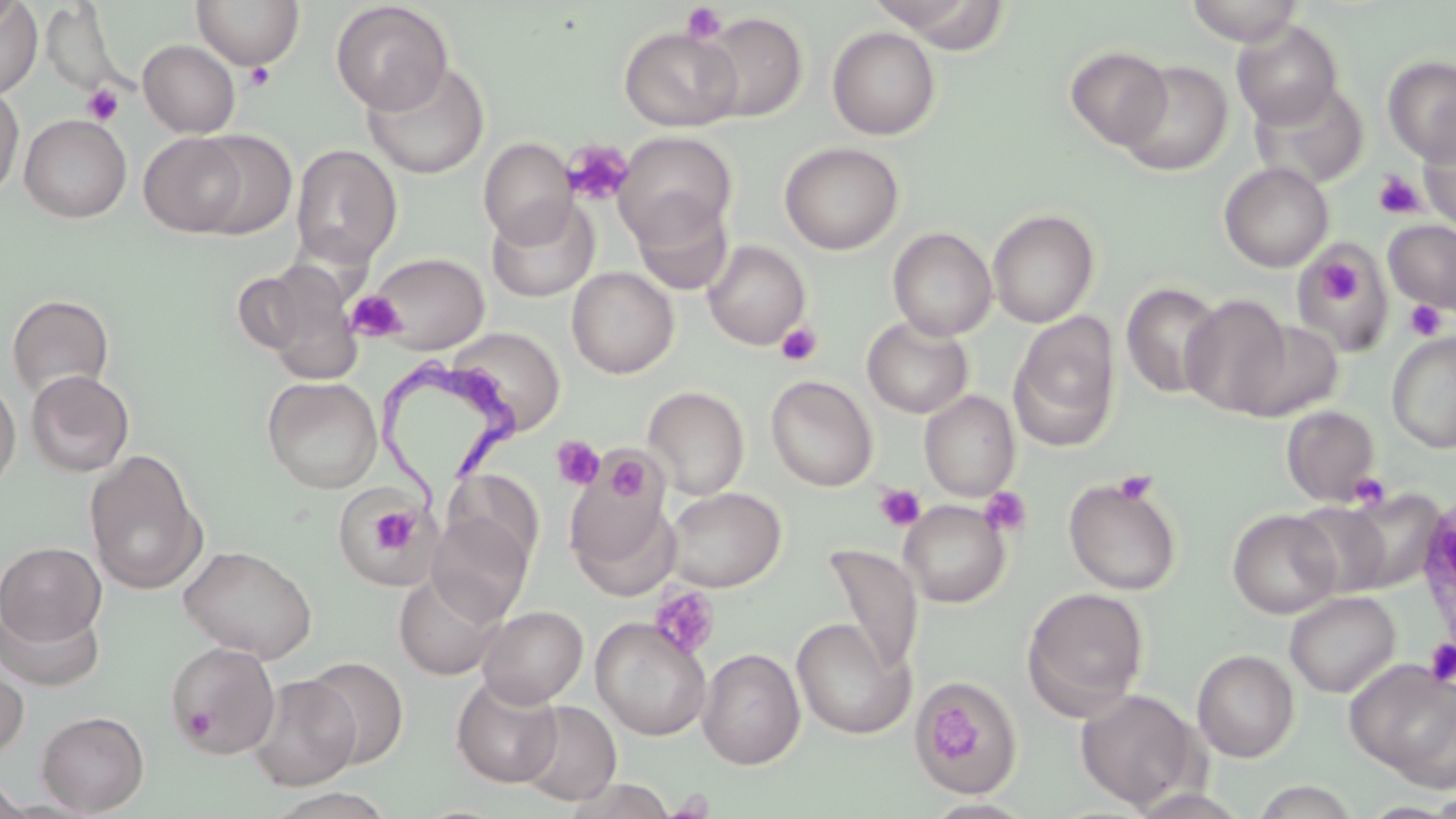 Approximate bounding boxes as named x1/y1/x2/y2 corners in pixels. Uninfected red blood cell locations: (x1=191, y1=0, x2=305, y2=70), (x1=867, y1=0, x2=1011, y2=50), (x1=0, y1=1, x2=42, y2=99), (x1=0, y1=1, x2=24, y2=31), (x1=331, y1=1, x2=453, y2=115), (x1=1183, y1=1, x2=1306, y2=46), (x1=43, y1=6, x2=122, y2=95), (x1=697, y1=11, x2=807, y2=123), (x1=1230, y1=19, x2=1344, y2=128), (x1=618, y1=26, x2=743, y2=131), (x1=827, y1=26, x2=941, y2=140), (x1=138, y1=40, x2=241, y2=138), (x1=1065, y1=45, x2=1173, y2=151), (x1=1383, y1=55, x2=1456, y2=165), (x1=361, y1=60, x2=490, y2=179), (x1=1118, y1=60, x2=1233, y2=176), (x1=1249, y1=80, x2=1368, y2=188), (x1=0, y1=84, x2=25, y2=202), (x1=19, y1=114, x2=132, y2=223), (x1=1418, y1=123, x2=1456, y2=233), (x1=190, y1=130, x2=297, y2=239), (x1=139, y1=132, x2=249, y2=237), (x1=613, y1=132, x2=737, y2=245), (x1=478, y1=138, x2=577, y2=245), (x1=779, y1=142, x2=904, y2=255), (x1=290, y1=144, x2=402, y2=268), (x1=1219, y1=162, x2=1333, y2=272), (x1=630, y1=193, x2=734, y2=296), (x1=485, y1=197, x2=599, y2=303), (x1=987, y1=208, x2=1099, y2=328), (x1=1383, y1=219, x2=1456, y2=314), (x1=888, y1=227, x2=997, y2=341), (x1=703, y1=240, x2=811, y2=350), (x1=1293, y1=248, x2=1393, y2=354), (x1=369, y1=252, x2=490, y2=353), (x1=242, y1=260, x2=363, y2=379), (x1=566, y1=267, x2=679, y2=379), (x1=1121, y1=281, x2=1225, y2=400), (x1=7, y1=292, x2=115, y2=399), (x1=1180, y1=294, x2=1292, y2=417), (x1=1008, y1=311, x2=1121, y2=452), (x1=862, y1=317, x2=973, y2=418), (x1=1231, y1=319, x2=1343, y2=422), (x1=448, y1=326, x2=566, y2=435), (x1=1387, y1=332, x2=1456, y2=453), (x1=25, y1=369, x2=135, y2=477), (x1=766, y1=375, x2=877, y2=492), (x1=263, y1=376, x2=383, y2=493), (x1=0, y1=377, x2=21, y2=496), (x1=641, y1=384, x2=874, y2=495), (x1=642, y1=385, x2=750, y2=500), (x1=919, y1=390, x2=1020, y2=501), (x1=1282, y1=406, x2=1381, y2=505), (x1=84, y1=449, x2=207, y2=595), (x1=565, y1=460, x2=672, y2=583), (x1=446, y1=471, x2=545, y2=572), (x1=1063, y1=476, x2=1183, y2=596), (x1=663, y1=486, x2=785, y2=592), (x1=1333, y1=487, x2=1445, y2=595), (x1=332, y1=488, x2=434, y2=590), (x1=899, y1=500, x2=1010, y2=607), (x1=1290, y1=501, x2=1395, y2=598), (x1=1227, y1=509, x2=1341, y2=618), (x1=427, y1=513, x2=532, y2=624), (x1=0, y1=542, x2=106, y2=647), (x1=179, y1=544, x2=317, y2=663), (x1=823, y1=544, x2=923, y2=676), (x1=394, y1=571, x2=505, y2=680), (x1=1022, y1=586, x2=1150, y2=716), (x1=1284, y1=591, x2=1400, y2=697), (x1=0, y1=602, x2=105, y2=691), (x1=476, y1=606, x2=588, y2=708), (x1=590, y1=617, x2=711, y2=741), (x1=791, y1=618, x2=913, y2=739), (x1=165, y1=641, x2=281, y2=758), (x1=697, y1=647, x2=805, y2=769), (x1=1192, y1=649, x2=1299, y2=762), (x1=302, y1=657, x2=409, y2=767), (x1=1346, y1=658, x2=1456, y2=787), (x1=0, y1=659, x2=29, y2=763), (x1=248, y1=674, x2=361, y2=790), (x1=451, y1=675, x2=563, y2=787), (x1=916, y1=680, x2=1018, y2=792), (x1=1076, y1=688, x2=1201, y2=810), (x1=516, y1=701, x2=621, y2=805), (x1=36, y1=710, x2=149, y2=815), (x1=0, y1=768, x2=29, y2=819), (x1=1249, y1=779, x2=1363, y2=818), (x1=263, y1=788, x2=398, y2=819). Platelet locations: (x1=680, y1=3, x2=729, y2=45), (x1=244, y1=62, x2=276, y2=91), (x1=82, y1=83, x2=124, y2=126), (x1=563, y1=140, x2=635, y2=206), (x1=1374, y1=170, x2=1426, y2=219), (x1=1318, y1=261, x2=1360, y2=306), (x1=346, y1=291, x2=407, y2=341), (x1=1403, y1=299, x2=1448, y2=342), (x1=776, y1=322, x2=822, y2=366), (x1=551, y1=436, x2=605, y2=490), (x1=605, y1=453, x2=651, y2=502), (x1=1112, y1=469, x2=1159, y2=505), (x1=1346, y1=472, x2=1391, y2=510), (x1=874, y1=484, x2=925, y2=532), (x1=979, y1=487, x2=1032, y2=538), (x1=363, y1=503, x2=422, y2=562), (x1=649, y1=586, x2=720, y2=659), (x1=1424, y1=638, x2=1456, y2=687), (x1=926, y1=701, x2=986, y2=764), (x1=180, y1=705, x2=218, y2=742). Trypanosoma brucei locations: (x1=381, y1=348, x2=532, y2=522). Slide-level diagnosis: Trypanosoma brucei. Thin blood smear. Captured at 1000x magnification. May-Grünwald-Giemsa stain. Image is 1456×819 pixels. Single field of view. Optical microscopy.